Name the parasite shown.
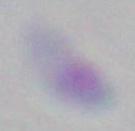
This is Toxoplasma gondii.

magnification = 1000x
modality = photomicrograph